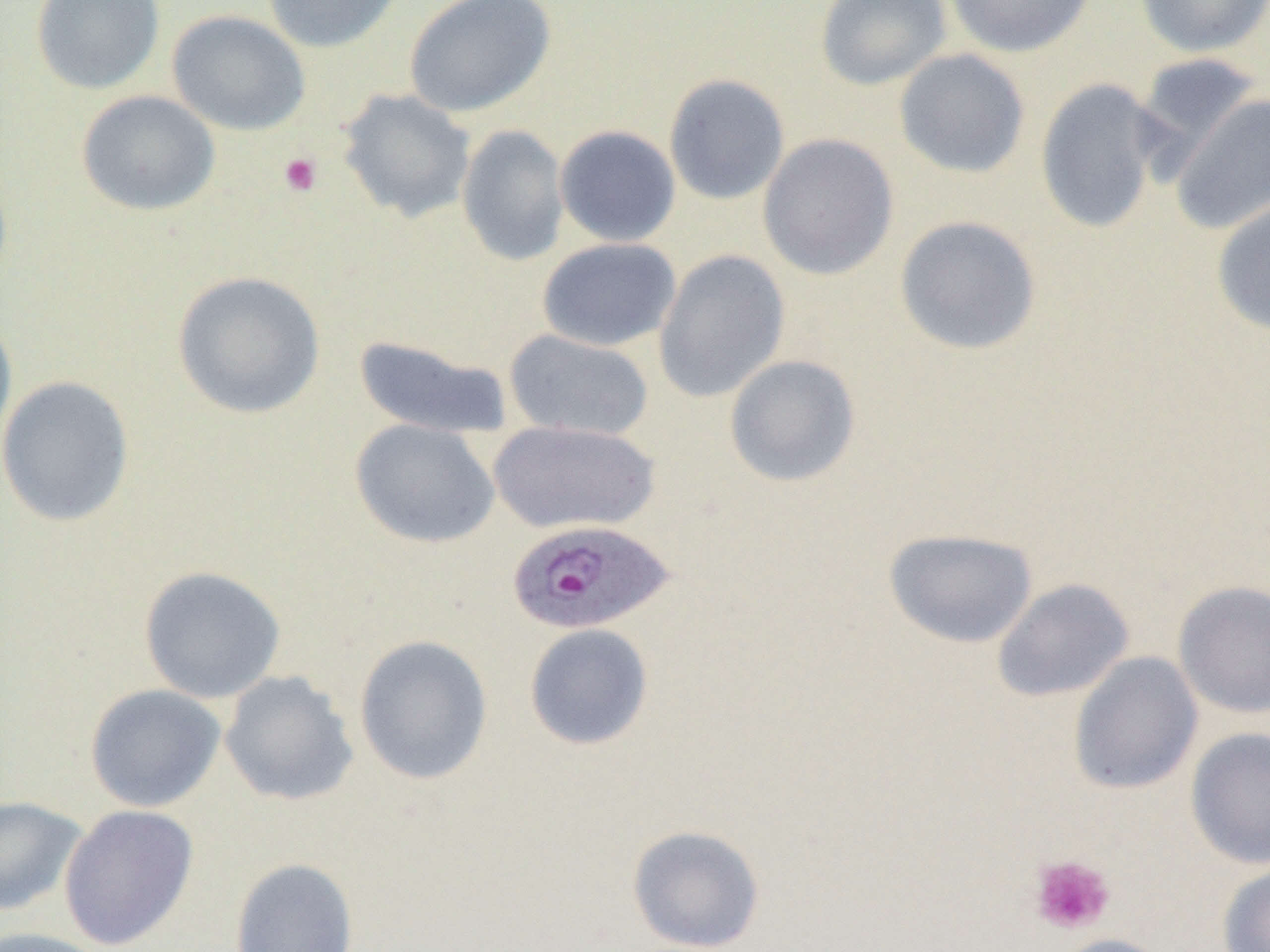
Summary:
  - Coordinate format: approximate bounding boxes as (x1, y1, x2, y2) in pixels
  - Platelet locations: (278, 152, 323, 197), (1029, 855, 1115, 935)
  - Uninfected red blood cell locations: (30, 0, 165, 95), (261, 0, 406, 53), (403, 0, 556, 118), (815, 0, 952, 91), (943, 0, 1097, 58), (1134, 0, 1270, 58), (166, 10, 311, 136), (893, 48, 1031, 179), (1133, 52, 1264, 166), (663, 73, 791, 205), (1034, 77, 1168, 234), (338, 88, 476, 223), (76, 90, 221, 216), (1169, 93, 1270, 234), (457, 124, 570, 266), (554, 125, 681, 247), (757, 133, 900, 281), (1210, 191, 1270, 336), (894, 214, 1042, 356), (537, 237, 681, 352), (653, 249, 790, 403), (171, 270, 326, 420), (0, 314, 18, 459), (504, 329, 654, 441), (353, 334, 514, 439), (724, 354, 861, 487), (0, 375, 135, 527), (349, 419, 500, 548), (489, 420, 661, 534), (883, 528, 1039, 648), (138, 565, 286, 703), (991, 577, 1134, 703), (1172, 580, 1270, 719), (523, 622, 655, 751), (353, 634, 493, 785), (1068, 651, 1203, 795), (219, 670, 360, 807), (84, 684, 227, 812), (1185, 726, 1270, 870), (0, 795, 89, 917), (59, 804, 199, 950), (626, 824, 766, 952), (229, 857, 359, 951), (1217, 861, 1270, 952), (0, 927, 115, 952), (1049, 933, 1178, 952)
  - Plasmodium ovale-infected red blood cell locations: (506, 519, 677, 636)
  - Slide-level diagnosis: Plasmodium ovale
  - Magnification: 1000x
  - Preparation: thin blood film
  - Modality: optical microscopy
  - Field of view: single
  - Image size: 1270×952 pixels